Assess this cell for malaria.
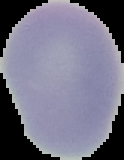

Uninfected.

Image is 124×160 pixels. Segmented cell region on a black background. From a thin blood smear.